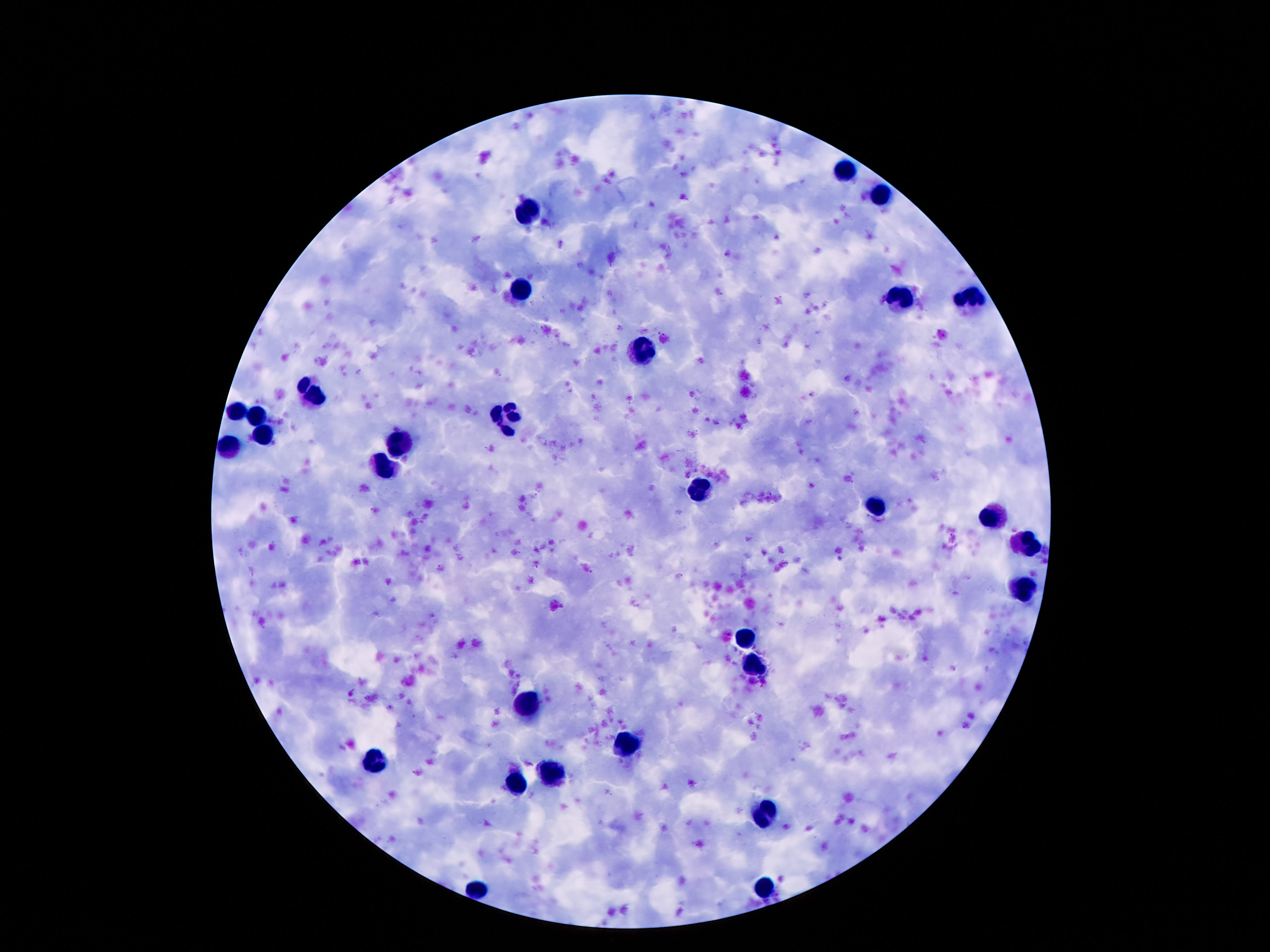 Approximate centers as {x, y} in pixels. Leukocyte locations: {848, 174}, {884, 198}, {527, 207}, {520, 291}, {973, 297}, {899, 302}, {641, 353}, {313, 394}, {507, 411}, {233, 414}, {257, 414}, {264, 434}, {406, 444}, {231, 448}, {382, 467}, {701, 490}, {876, 510}, {992, 517}, {1029, 543}, {1022, 588}, {751, 638}, {523, 708}, {628, 741}, {376, 761}, {554, 776}, {518, 781}, {765, 809}, {770, 884}, {479, 890}. Smartphone photograph taken through the microscope eyepiece. Image is 1270×952 pixels. 100x magnification. One field from this slide. Patient malaria status: not infected. Thick blood smear. Giemsa-stained preparation.